Identify the parasite.
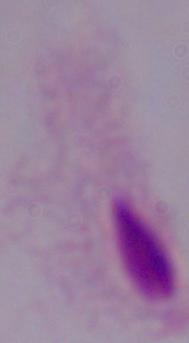
A trichomonad.

Captured at 1000x magnification. Micrograph.